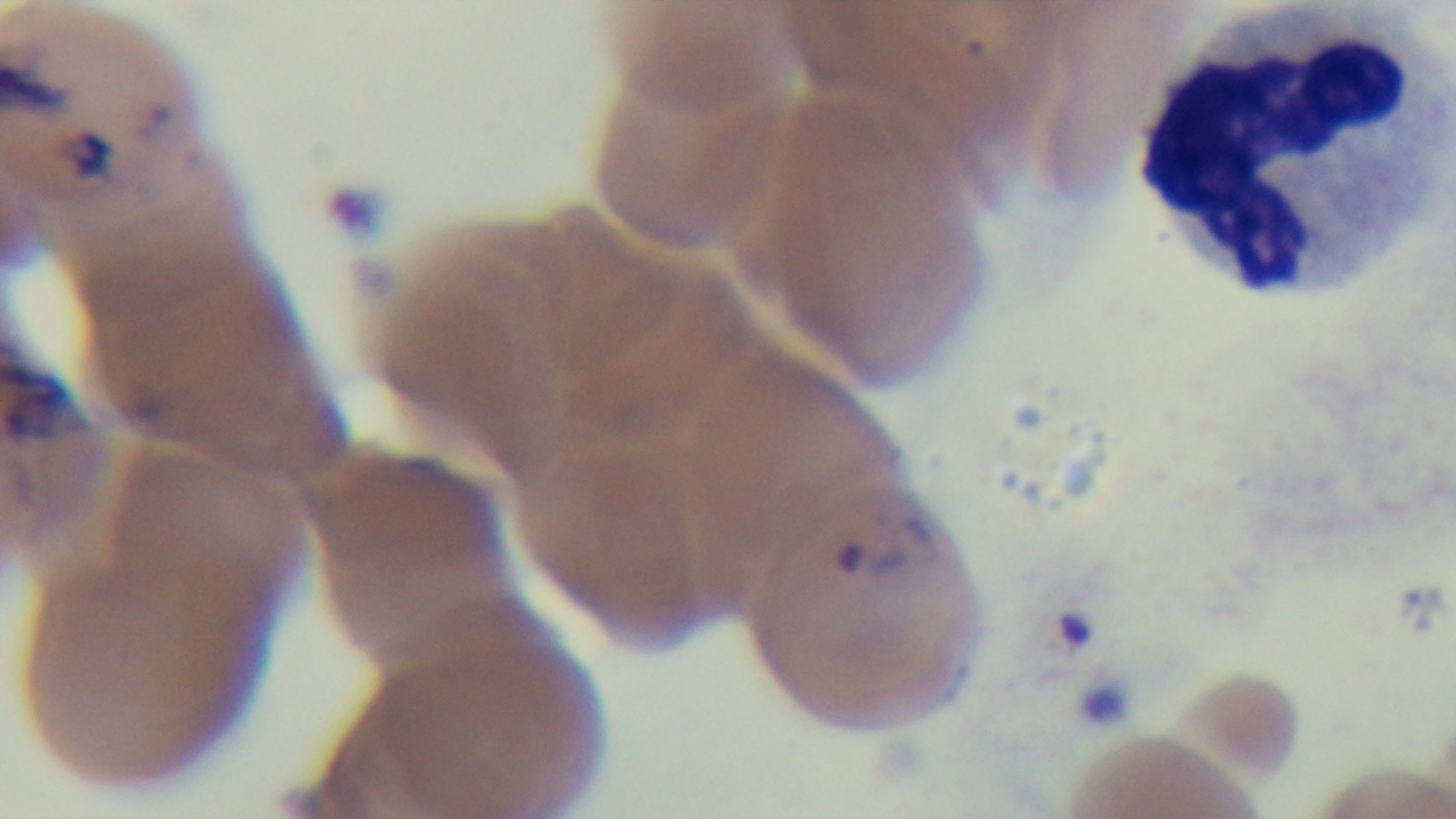
{
  "objective": "100x oil immersion",
  "modality": "light microscopy",
  "malaria_status": "positive",
  "capture": "mounted 4K digital camera",
  "stain": "Giemsa",
  "preparation": "thin smear",
  "field_of_view": "one from the slide"
}